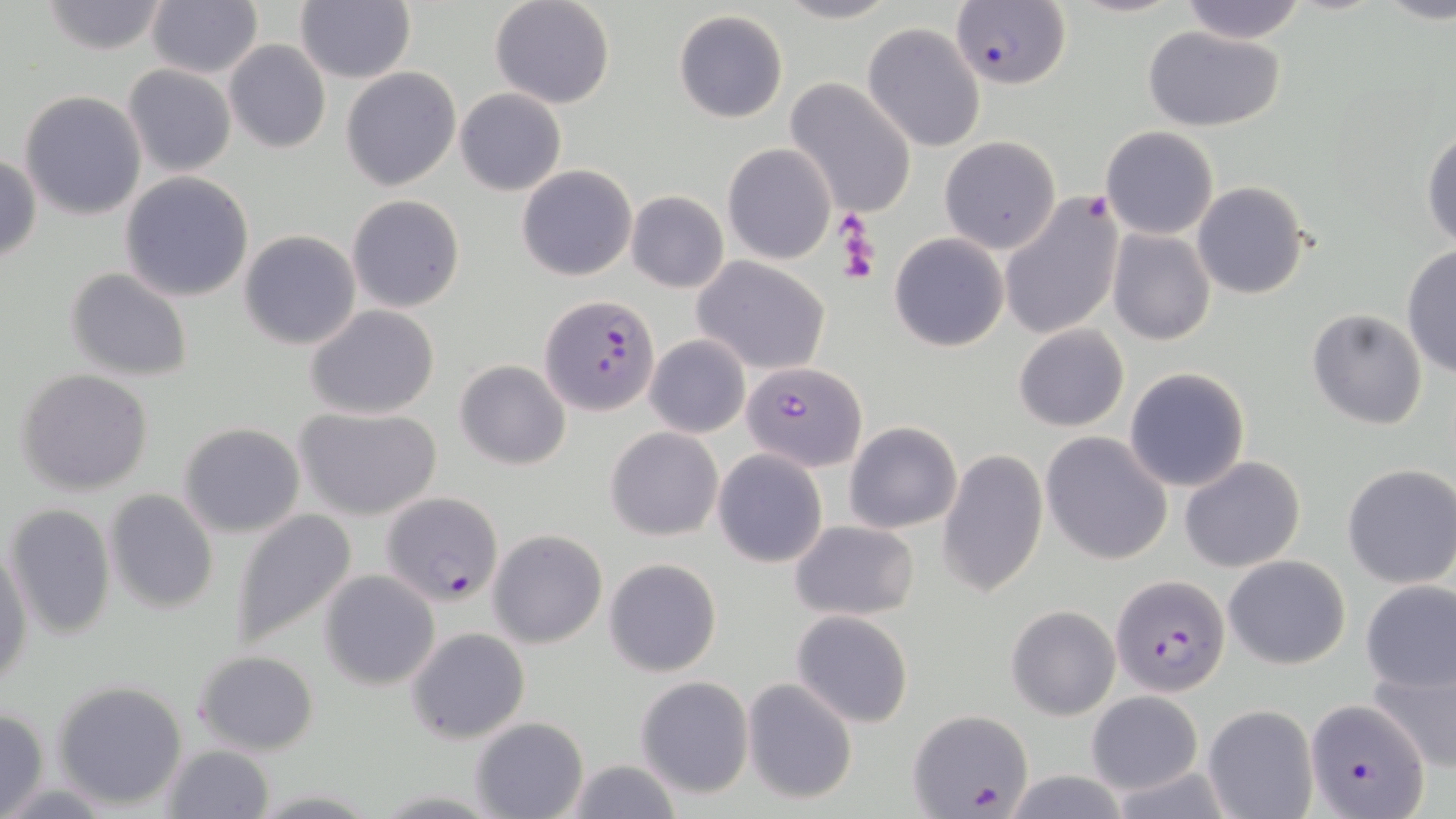
slide-level diagnosis = Plasmodium falciparum
uninfected red blood cell locations = approximate bounding boxes as (x1,y1)-(x2,y2) corner pairs in pixels: (297,0)-(415,84), (489,0)-(616,109), (776,0)-(898,24), (40,1)-(170,53), (1178,1)-(1309,42), (148,2)-(262,78), (673,10)-(788,123), (863,22)-(986,153), (1141,25)-(1286,130), (225,40)-(329,154), (123,65)-(236,178), (341,67)-(461,192), (784,78)-(918,218), (455,88)-(566,196), (19,90)-(148,220), (1101,125)-(1219,239), (1422,128)-(1455,252), (940,136)-(1061,253), (722,143)-(835,265), (0,152)-(41,265), (516,163)-(636,281), (120,172)-(255,302), (1193,179)-(1310,300), (626,190)-(728,293), (998,193)-(1125,342), (347,195)-(466,313), (1106,228)-(1215,346), (239,230)-(361,350), (889,232)-(1010,352), (1401,246)-(1455,377), (691,256)-(831,374), (66,267)-(193,382), (305,305)-(440,419), (1307,308)-(1430,429), (1014,324)-(1129,432), (644,334)-(751,438), (454,359)-(571,470), (1123,367)-(1251,493), (17,369)-(155,495), (292,404)-(443,520), (178,422)-(306,537), (844,422)-(962,533), (606,426)-(724,541), (1041,432)-(1172,565), (713,448)-(828,568), (938,449)-(1048,598), (1179,454)-(1307,573), (1341,463)-(1456,589), (104,490)-(218,612), (5,503)-(115,639), (228,507)-(358,650), (788,519)-(918,620), (488,529)-(607,649), (1,541)-(33,689), (1222,555)-(1350,669), (604,557)-(722,677), (320,570)-(440,689), (1361,580)-(1455,693), (1006,604)-(1121,720), (791,610)-(914,728), (406,627)-(530,744), (192,650)-(316,755), (1369,663)-(1454,772), (635,676)-(755,799), (741,677)-(857,805), (52,679)-(189,809), (1087,691)-(1202,794), (1202,704)-(1319,819), (0,706)-(49,818), (471,716)-(589,819), (160,744)-(274,819), (561,757)-(684,818), (997,770)-(1134,819)
image size = 1456×819 pixels
Plasmodium falciparum-infected red blood cell locations = approximate bounding boxes as (x1,y1)-(x2,y2) corner pairs in pixels: (950,1)-(1069,87), (543,295)-(658,418), (743,360)-(866,471), (377,492)-(507,607), (1110,574)-(1231,696), (1307,699)-(1431,819), (906,709)-(1032,817)
magnification = 1000x
preparation = thin blood film
modality = optical microscopy
field of view = one of a larger specimen
platelet locations = approximate bounding boxes as (x1,y1)-(x2,y2) corner pairs in pixels: (839,221)-(880,286)
stain = May-Grünwald-Giemsa